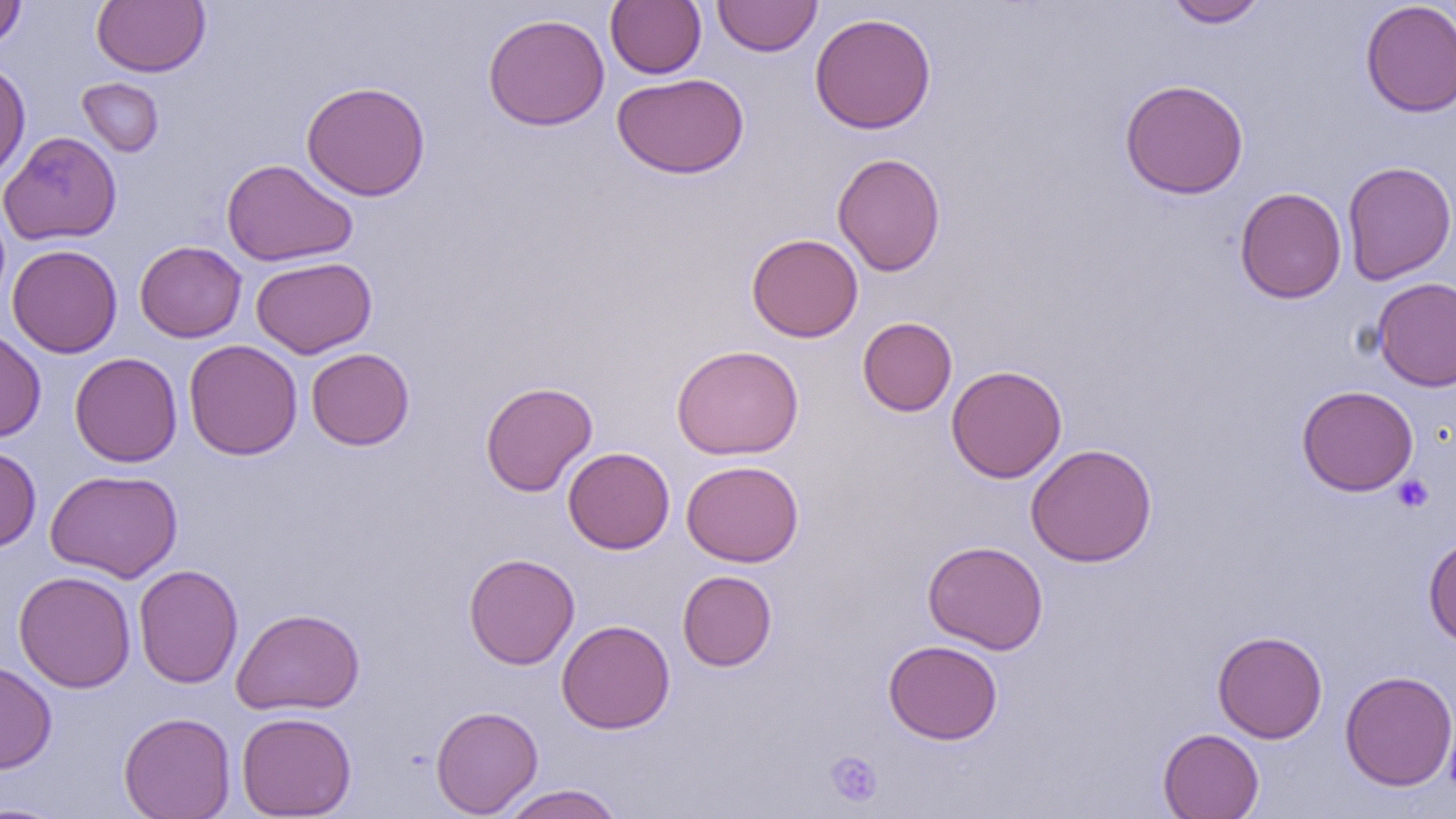
slide-level diagnosis = no evidence of blood parasites
uninfected red blood cell locations = approximate bounding boxes as (x1,y1)-(x2,y2) corner pairs in pixels: (91,0)-(210,77), (605,0)-(706,78), (712,0)-(821,57), (1163,0)-(1269,28), (1360,0)-(1456,117), (0,1)-(27,51), (809,12)-(937,134), (482,13)-(610,131), (0,61)-(31,184), (612,72)-(749,179), (77,77)-(164,157), (1119,78)-(1249,199), (301,81)-(431,201), (0,131)-(123,246), (832,152)-(946,276), (221,159)-(358,267), (1341,160)-(1456,285), (1235,187)-(1346,303), (746,233)-(863,342), (135,241)-(247,342), (7,244)-(122,358), (250,256)-(377,358), (1372,277)-(1456,392), (857,316)-(957,417), (0,329)-(46,442), (184,339)-(303,460), (671,344)-(804,460), (305,348)-(415,450), (70,352)-(183,467), (946,365)-(1067,483), (480,381)-(597,496), (1296,384)-(1419,496), (1025,443)-(1157,567), (0,445)-(41,552), (562,446)-(675,554), (681,460)-(804,567), (44,468)-(183,583), (1423,534)-(1456,648), (922,540)-(1048,655), (463,552)-(580,669), (134,564)-(243,688), (13,570)-(137,693), (677,570)-(777,671), (231,606)-(365,715), (556,619)-(675,734), (1212,630)-(1328,743), (883,639)-(1003,745), (0,660)-(57,773), (1340,670)-(1456,791), (431,705)-(543,817), (118,711)-(236,819), (236,711)-(357,818), (1158,728)-(1264,819), (499,784)-(625,819), (0,801)-(69,818)
preparation = thin blood smear
field of view = single
image size = 1456×819 pixels
magnification = 1000x
platelet locations = approximate bounding boxes as (x1,y1)-(x2,y2) corner pairs in pixels: (1392,474)-(1434,512), (825,750)-(883,808)
modality = optical microscopy